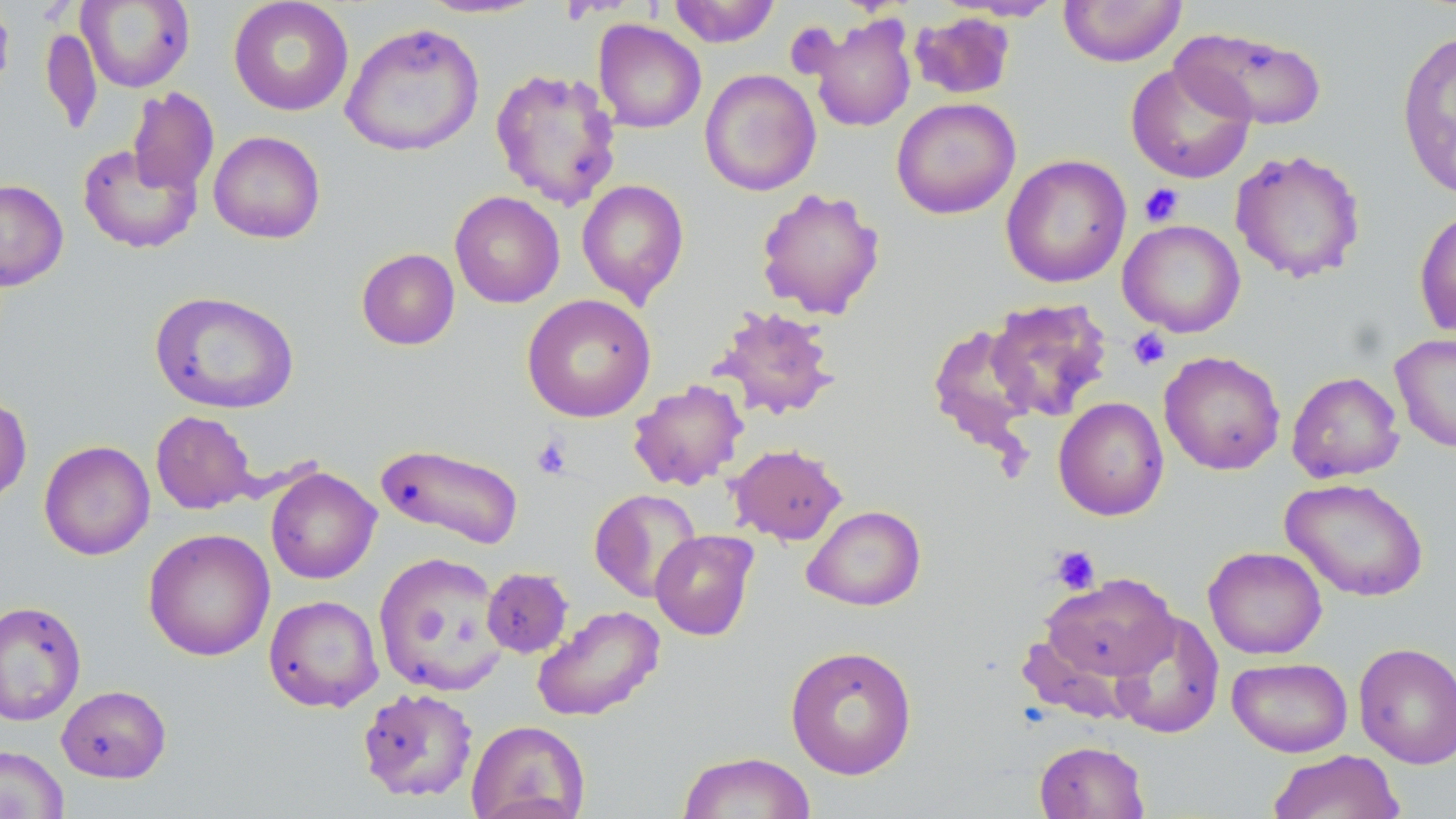

Approximate bounding boxes as (x1, y1, x2, y2) in pixels. Platelet locations: (1139, 183, 1184, 227), (1128, 328, 1171, 370), (532, 435, 573, 479), (1049, 545, 1100, 594). Uninfected red blood cell locations: (228, 0, 354, 117), (418, 0, 547, 19), (668, 0, 781, 47), (1059, 0, 1187, 67), (0, 1, 15, 102), (77, 1, 195, 92), (910, 11, 1016, 99), (808, 13, 917, 132), (593, 20, 706, 133), (339, 22, 485, 158), (40, 26, 103, 135), (1171, 26, 1328, 131), (1396, 29, 1456, 200), (1125, 62, 1256, 183), (489, 67, 622, 210), (699, 68, 821, 196), (127, 87, 219, 196), (891, 97, 1021, 219), (209, 131, 325, 244), (77, 143, 201, 254), (1229, 148, 1367, 284), (1000, 154, 1132, 288), (576, 178, 690, 307), (0, 179, 69, 291), (755, 186, 885, 319), (449, 191, 565, 308), (1413, 207, 1456, 340), (1118, 219, 1245, 338), (356, 248, 460, 350), (148, 290, 301, 415), (522, 293, 656, 423), (984, 297, 1113, 422), (709, 304, 840, 421), (928, 323, 1040, 455), (1390, 332, 1456, 453), (1159, 350, 1286, 475), (1287, 370, 1404, 483), (628, 379, 748, 491), (0, 392, 32, 506), (1053, 396, 1169, 521), (151, 411, 256, 514), (38, 440, 155, 561), (375, 441, 524, 550), (728, 443, 848, 545), (265, 467, 380, 584), (1280, 477, 1429, 601), (589, 489, 702, 602), (802, 504, 926, 611), (143, 528, 275, 661), (650, 530, 759, 640), (1203, 546, 1327, 659), (373, 551, 508, 696), (482, 567, 573, 658), (1039, 573, 1178, 684), (264, 594, 383, 712), (0, 600, 87, 726), (532, 605, 665, 722), (1110, 611, 1225, 738), (1353, 641, 1456, 768), (785, 644, 918, 779), (1227, 656, 1353, 757), (56, 684, 172, 783), (357, 687, 478, 802), (466, 720, 590, 819), (1034, 740, 1150, 819), (0, 744, 70, 819), (1267, 750, 1405, 819), (677, 751, 816, 819). Slide-level diagnosis: negative for blood parasites. Thin blood smear. May-Grünwald-Giemsa-stained preparation. Single field of view. Captured at 1000x magnification. Image is 1456×819 pixels. Optical microscopy.